State the blood parasite species.
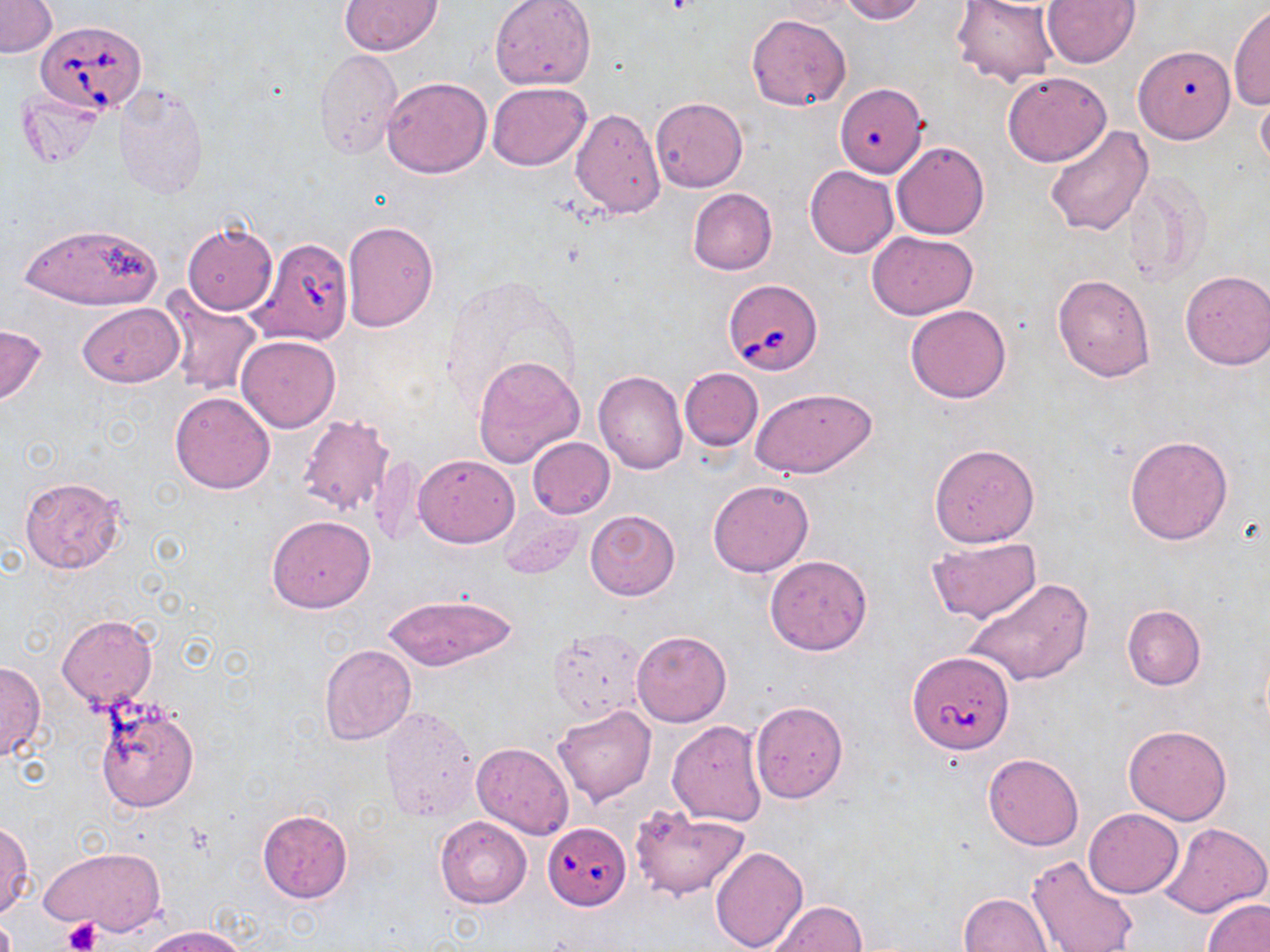
Babesia divergens.

uninfected red blood cell locations = approximate bounding boxes as named x1/y1/x2/y2 corners in pixels: (x1=339, y1=0, x2=443, y2=55), (x1=838, y1=0, x2=926, y2=23), (x1=951, y1=0, x2=1059, y2=88), (x1=1, y1=1, x2=57, y2=58), (x1=490, y1=1, x2=596, y2=91), (x1=1041, y1=1, x2=1141, y2=69), (x1=1228, y1=3, x2=1270, y2=111), (x1=747, y1=14, x2=852, y2=110), (x1=1133, y1=45, x2=1235, y2=143), (x1=315, y1=50, x2=402, y2=160), (x1=1002, y1=71, x2=1110, y2=166), (x1=382, y1=77, x2=492, y2=178), (x1=115, y1=82, x2=209, y2=200), (x1=489, y1=83, x2=589, y2=168), (x1=834, y1=86, x2=930, y2=180), (x1=1256, y1=89, x2=1270, y2=176), (x1=650, y1=97, x2=747, y2=192), (x1=570, y1=107, x2=665, y2=218), (x1=1044, y1=125, x2=1153, y2=236), (x1=892, y1=141, x2=989, y2=239), (x1=806, y1=166, x2=899, y2=258), (x1=1120, y1=171, x2=1209, y2=285), (x1=688, y1=188, x2=777, y2=276), (x1=342, y1=220, x2=438, y2=331), (x1=15, y1=221, x2=164, y2=310), (x1=180, y1=221, x2=278, y2=315), (x1=868, y1=230, x2=977, y2=319), (x1=246, y1=237, x2=358, y2=347), (x1=1180, y1=270, x2=1270, y2=370), (x1=1053, y1=273, x2=1156, y2=382), (x1=165, y1=294, x2=262, y2=398), (x1=78, y1=302, x2=183, y2=388), (x1=905, y1=303, x2=1013, y2=404), (x1=0, y1=323, x2=48, y2=407), (x1=237, y1=334, x2=340, y2=432), (x1=472, y1=355, x2=585, y2=467), (x1=679, y1=367, x2=764, y2=450), (x1=593, y1=370, x2=688, y2=474), (x1=751, y1=387, x2=877, y2=479), (x1=170, y1=390, x2=275, y2=494), (x1=296, y1=413, x2=395, y2=517), (x1=1124, y1=435, x2=1233, y2=545), (x1=527, y1=437, x2=615, y2=519), (x1=929, y1=444, x2=1039, y2=547), (x1=369, y1=454, x2=425, y2=546), (x1=413, y1=454, x2=519, y2=547), (x1=19, y1=475, x2=127, y2=574), (x1=707, y1=478, x2=814, y2=577), (x1=498, y1=506, x2=584, y2=580), (x1=585, y1=510, x2=679, y2=600), (x1=266, y1=516, x2=375, y2=613), (x1=925, y1=537, x2=1043, y2=625), (x1=765, y1=555, x2=873, y2=656), (x1=962, y1=577, x2=1093, y2=688), (x1=381, y1=593, x2=517, y2=671), (x1=1121, y1=604, x2=1205, y2=690), (x1=57, y1=614, x2=157, y2=711), (x1=546, y1=627, x2=646, y2=722), (x1=631, y1=630, x2=732, y2=726), (x1=318, y1=643, x2=417, y2=745), (x1=0, y1=660, x2=46, y2=761), (x1=91, y1=694, x2=202, y2=813), (x1=750, y1=700, x2=848, y2=804), (x1=552, y1=704, x2=656, y2=805), (x1=379, y1=705, x2=478, y2=823), (x1=667, y1=721, x2=766, y2=827), (x1=1123, y1=724, x2=1232, y2=825), (x1=472, y1=743, x2=574, y2=838), (x1=983, y1=753, x2=1085, y2=851), (x1=628, y1=805, x2=752, y2=900), (x1=257, y1=809, x2=353, y2=903), (x1=1083, y1=809, x2=1182, y2=897), (x1=434, y1=815, x2=532, y2=909), (x1=1159, y1=821, x2=1270, y2=917), (x1=0, y1=822, x2=33, y2=917), (x1=670, y1=823, x2=786, y2=941), (x1=709, y1=845, x2=807, y2=952), (x1=38, y1=847, x2=169, y2=936), (x1=1026, y1=854, x2=1138, y2=952), (x1=959, y1=892, x2=1054, y2=952), (x1=1203, y1=897, x2=1268, y2=952), (x1=769, y1=900, x2=866, y2=951), (x1=143, y1=925, x2=249, y2=952)
image size = 1270×952 pixels
magnification = 1000x
Babesia divergens-infected red blood cell locations = approximate bounding boxes as named x1/y1/x2/y2 corners in pixels: (x1=35, y1=21, x2=148, y2=115), (x1=721, y1=279, x2=823, y2=375), (x1=907, y1=652, x2=1015, y2=754), (x1=542, y1=822, x2=631, y2=911)
modality = optical microscopy
stain = May-Grünwald-Giemsa
field of view = single
preparation = thin blood smear
platelet locations = approximate bounding boxes as named x1/y1/x2/y2 corners in pixels: (x1=63, y1=917, x2=100, y2=951)